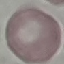

Summary:
  - Malaria status: uninfected
  - Preparation: thin blood smear
  - Stain: Giemsa
  - Image type: cell patch, automatically extracted from a larger field of view and resized to 64 × 64 pixels
  - Capture: smartphone camera at the microscope eyepiece